Identify the cell.
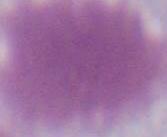
This is an erythrocyte.

Summary:
  - Magnification: 1000x
  - Modality: micrograph